Give the position of every Plasmodium parasite.
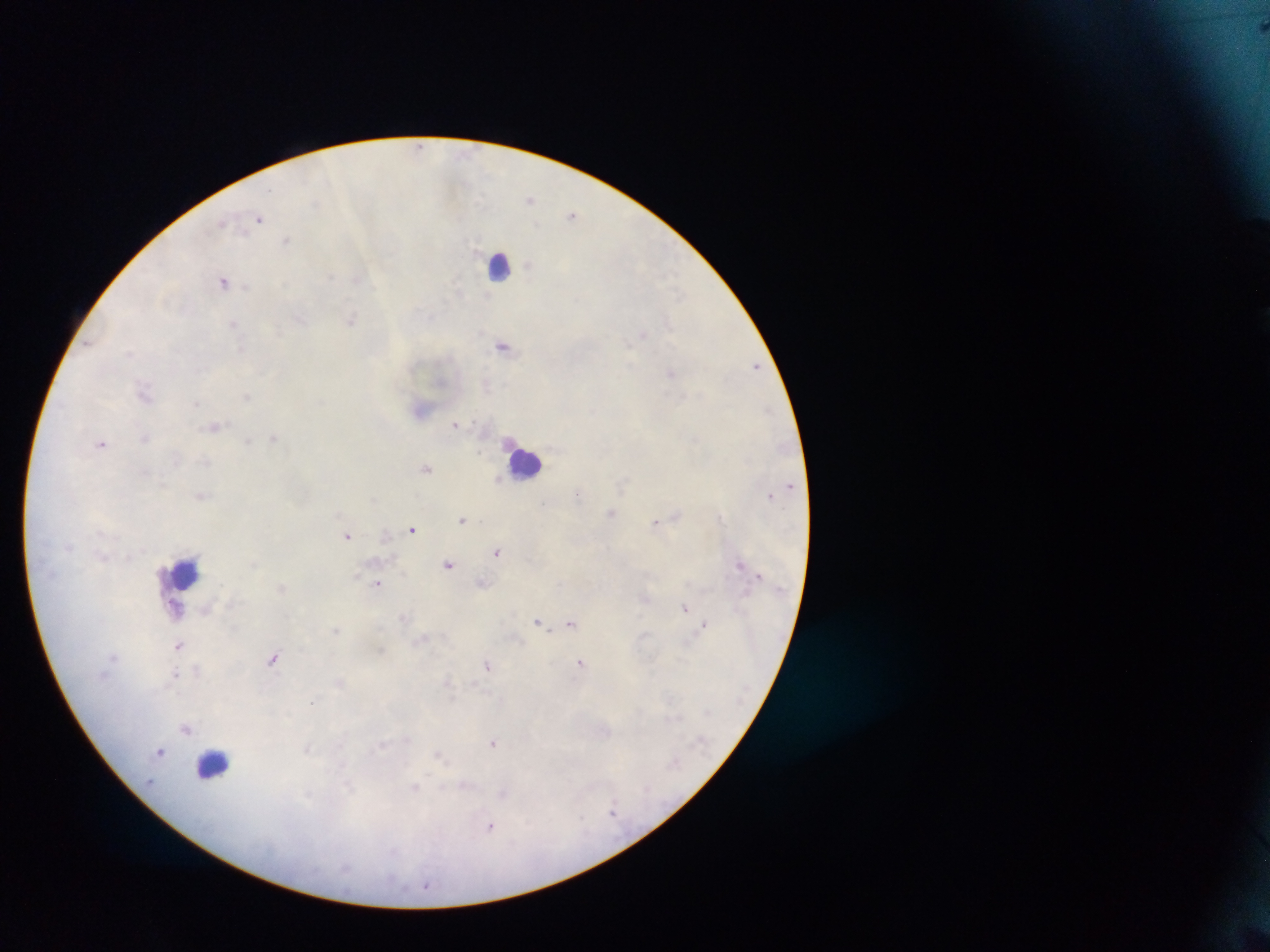

Approximate centers as [x, y] in pixels.
Plasmodium parasites: [1262, 27], [418, 146], [530, 199], [573, 215], [259, 218], [287, 241], [225, 280], [352, 319], [235, 324], [643, 334], [504, 345], [755, 366], [671, 374], [145, 392], [421, 409], [456, 424], [215, 425], [146, 438], [274, 438], [248, 440], [102, 443], [427, 469], [498, 479], [201, 495], [578, 495], [772, 495], [612, 512], [463, 518], [656, 521], [412, 528], [347, 535], [497, 551], [448, 564], [741, 565], [482, 583], [378, 584], [281, 588], [645, 598], [685, 607], [405, 616], [571, 622], [538, 623], [704, 624], [336, 630], [424, 639], [180, 645], [274, 658], [581, 663], [488, 665], [177, 676], [340, 682], [448, 682], [186, 727], [494, 742], [307, 748], [161, 751], [440, 755], [416, 789], [614, 810], [489, 826], [425, 885].

Summary:
  - Leukocyte locations: [499, 264], [526, 463], [183, 573], [179, 606], [213, 765]
  - Preparation: thick blood film
  - Country: Ghana
  - Image size: 1270×952 pixels
  - Capture: mobile-phone photograph through a microscope
  - Field of view: single